Report the malaria status of this cell.
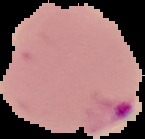

Parasitized.

image type = cell region segmented out of the field of view; surrounding area masked to black
preparation = thin blood smear
image size = 145×139 pixels